Report the malaria status of this cell.
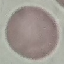
It is uninfected.

capture = smartphone camera at the microscope eyepiece
preparation = thin smear
image type = cell patch, automatically extracted from a larger field of view and resized to 64 × 64 pixels
stain = Giemsa